Classify this cell by malaria status.
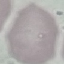

Uninfected.

{
  "preparation": "thin blood smear",
  "capture": "smartphone camera at the microscope eyepiece",
  "image_type": "automatically extracted cell patch, resized to 64 × 64 pixels",
  "stain": "Giemsa"
}